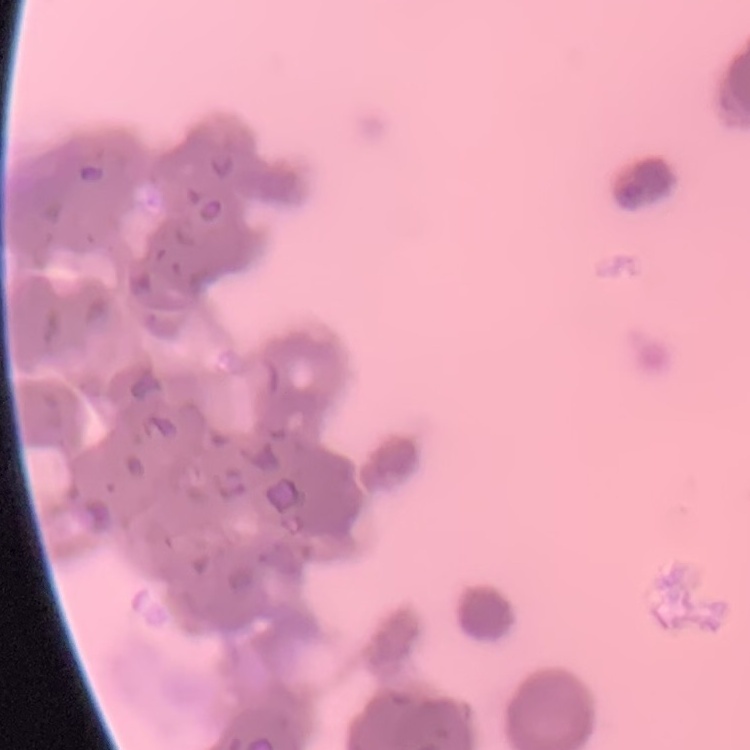 The erythrocytes show rouleaux formation. Square crop of a larger photomicrograph. Stained with either Field's or Giemsa. Thin blood smear.